Assess this cell for malaria.
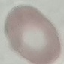
Uninfected.

Automatically extracted cell patch, resized to 64 × 64 pixels. Acquired by smartphone through the microscope eyepiece. Thin blood smear. Giemsa-stained preparation.